Locate malaria parasites and leukocytes.
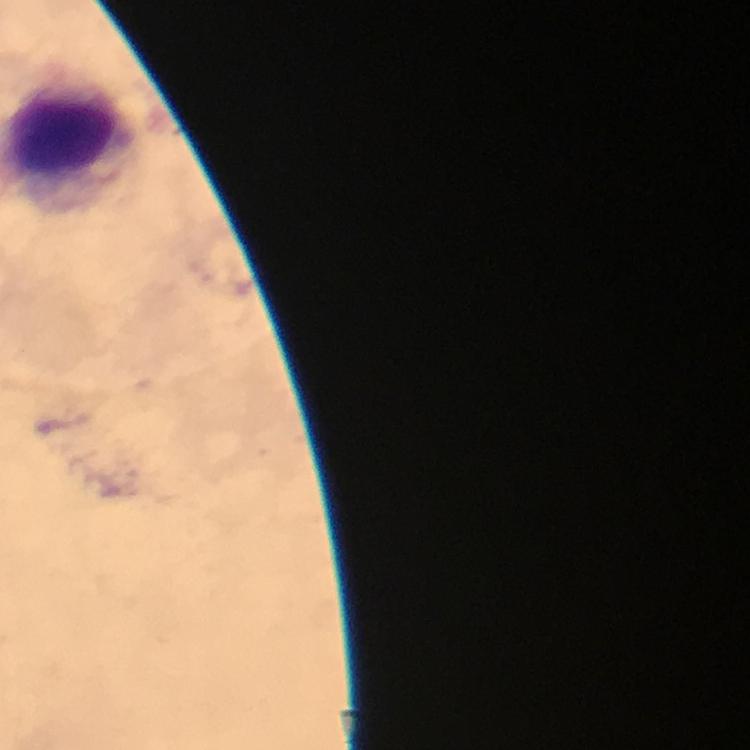
No malaria parasites seen.
Approximate object centers, in pixels from the top-left corner.
Leukocytes: (x=65, y=144).

Summary:
  - Preparation: thick smear
  - Immersion oil: used
  - Image size: 750×750 pixels
  - Context: from a diagnostic examination for malaria
  - Capture: smartphone photograph through a microscope
  - Cropped from: a single field of view
  - Magnification: 100x
  - Stain: Giemsa